State the preparation type.
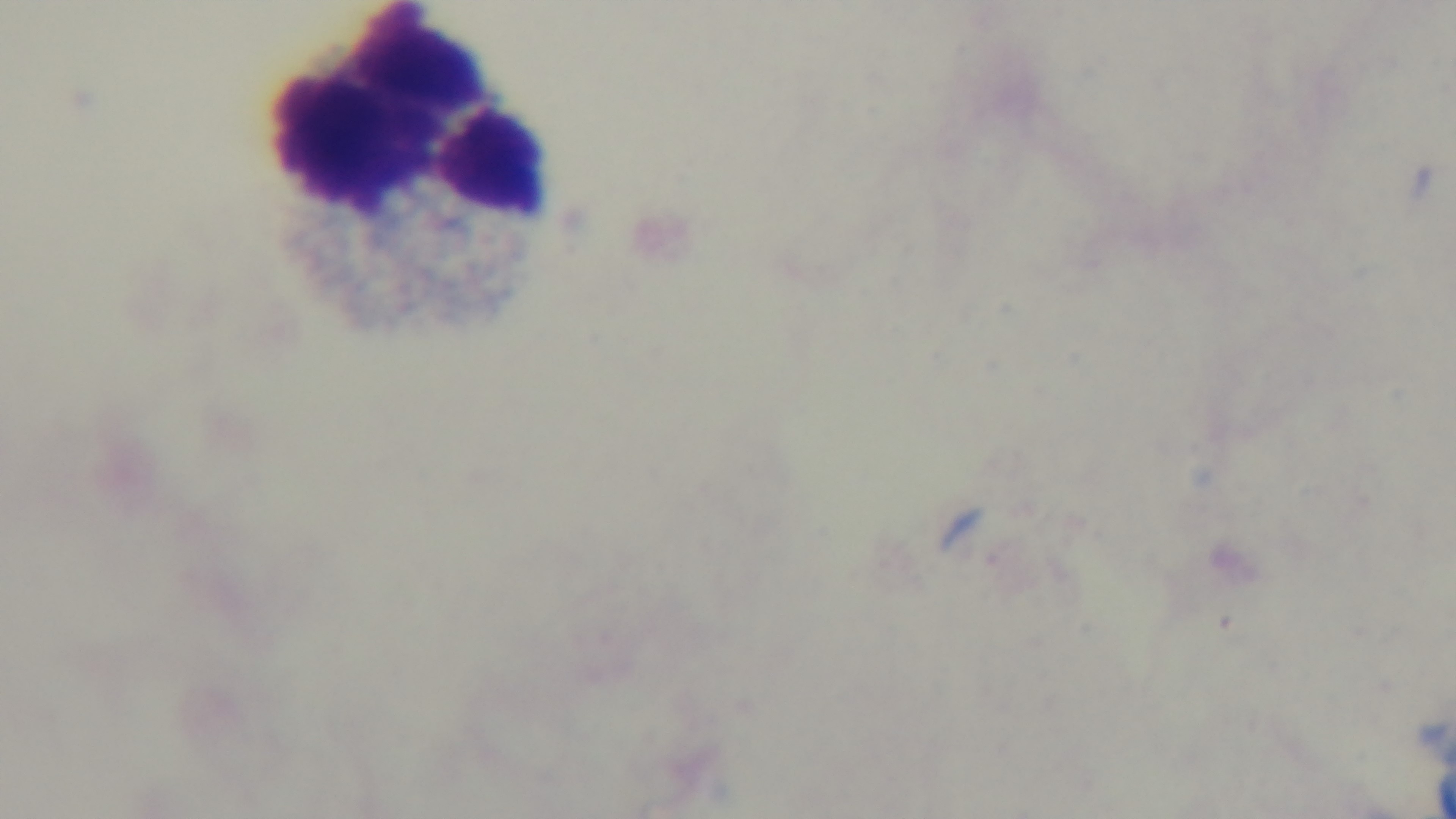

Thick.

modality: light microscopy
field_of_view: one from the slide
malaria_status: negative
capture: mounted 4K digital camera
stain: Giemsa
objective: 100x oil immersion